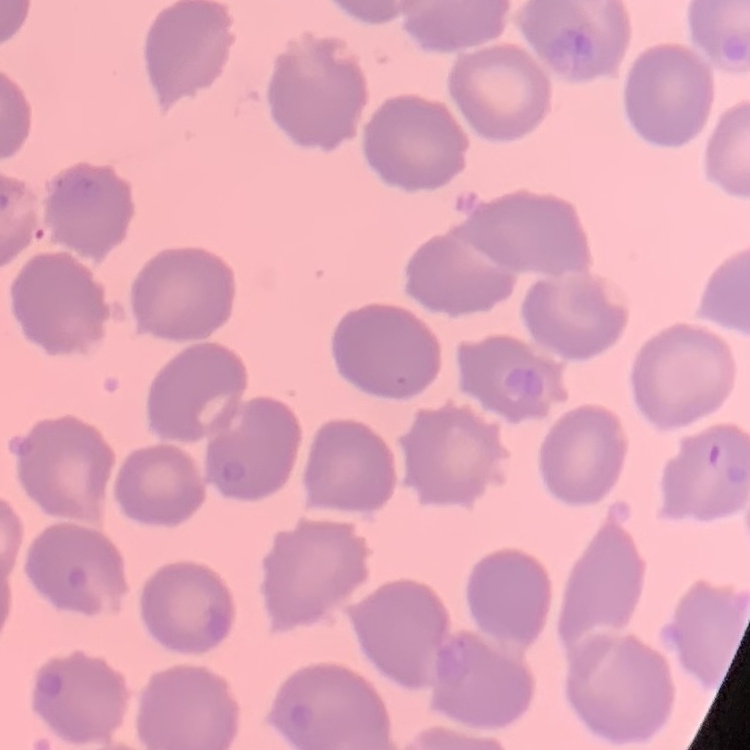

erythrocyte_morphology: no rouleaux formation
image_type: one tile cut from a larger photomicrograph
preparation: thin blood film
stain: Field's or Giemsa